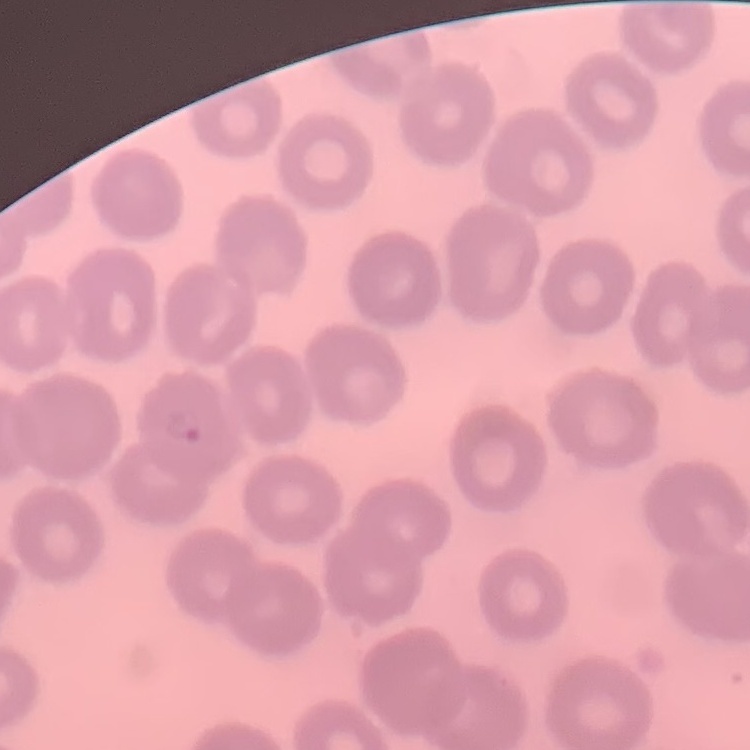

The erythrocytes show no rouleaux formation. Thin peripheral smear. Field's or Giemsa stain. One tile cut from a larger photomicrograph.